Classify the preparation.
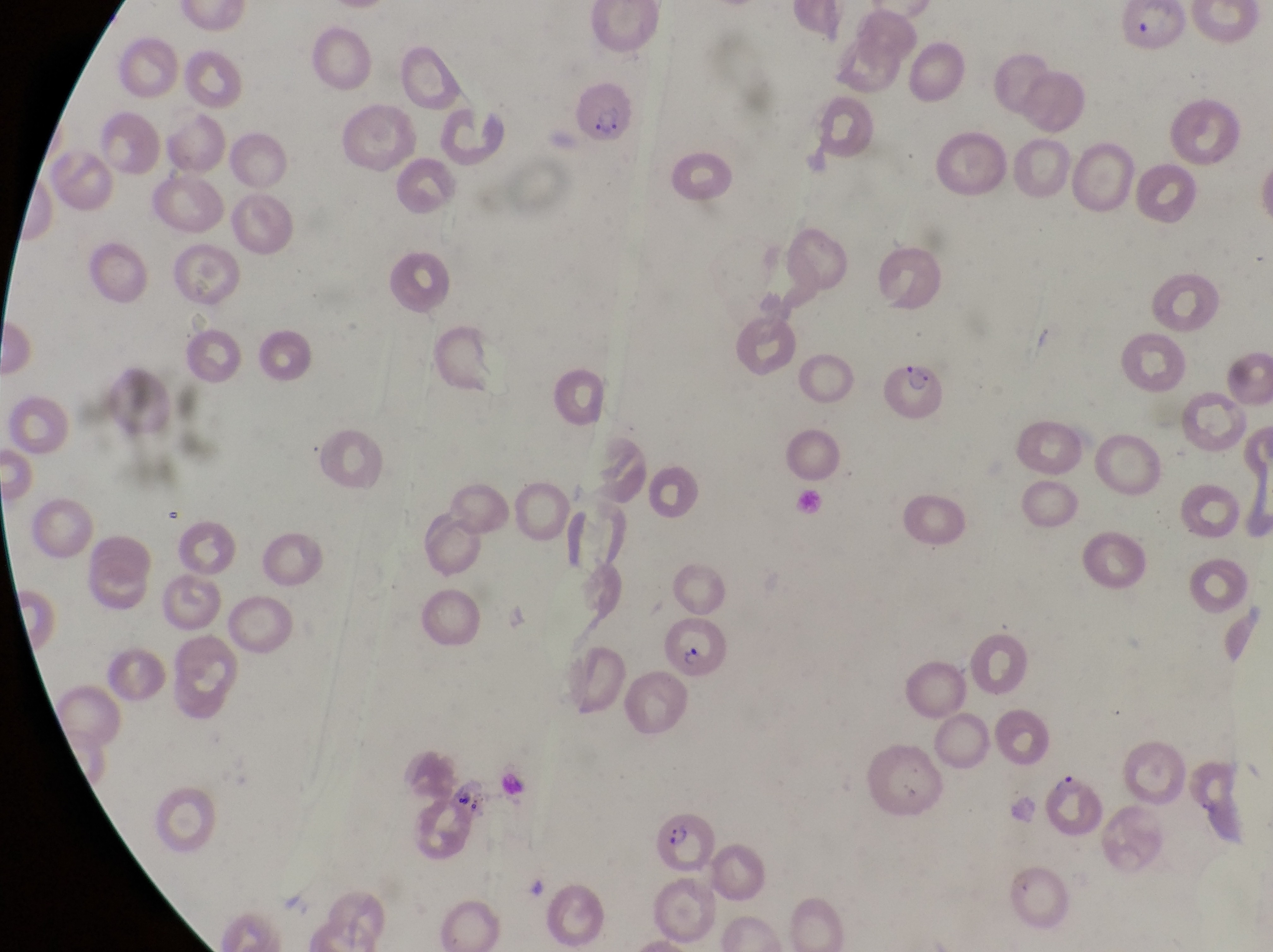
Thin blood smear.

Approximate bounding boxes as (left, top, right, bottom) in pixels. Parasitised red blood cell locations: (882, 354, 957, 424), (654, 621, 734, 688), (1048, 762, 1105, 844), (647, 794, 712, 872), (998, 857, 1067, 925). Image is 1273×952 pixels. Sample from Uganda. Captured by a smartphone held over the eyepiece of an Olympus CX-23 microscope. At a magnification of 1000x. One field of view.